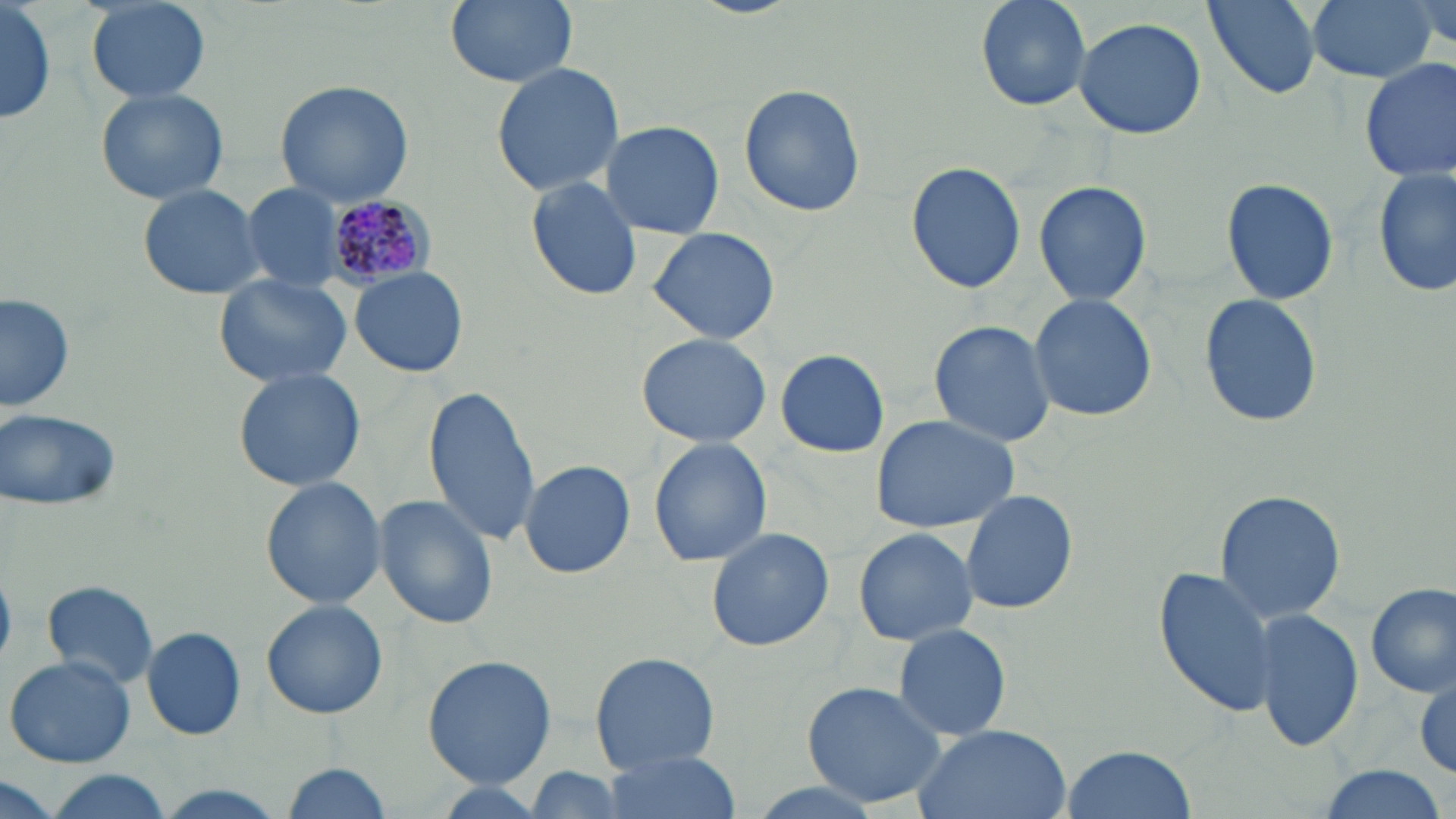
Summary:
  - Coordinate format: approximate bounding boxes as (x1,y1)-(x2,y2) corner pairs in pixels
  - Uninfected red blood cell locations: (1,0)-(56,127), (444,0)-(582,90), (974,0)-(1091,109), (1203,0)-(1327,98), (1303,0)-(1440,84), (1407,0)-(1453,52), (84,1)-(212,104), (1072,16)-(1209,138), (1358,57)-(1455,184), (489,60)-(625,199), (274,78)-(415,208), (737,85)-(867,218), (94,86)-(229,206), (599,120)-(725,239), (906,161)-(1026,292), (1372,168)-(1455,298), (525,175)-(645,303), (1220,176)-(1340,306), (1033,179)-(1153,307), (136,181)-(269,301), (239,183)-(353,292), (647,226)-(780,346), (350,266)-(470,378), (212,275)-(355,389), (2,291)-(75,417), (1026,293)-(1159,423), (1198,293)-(1323,430), (927,319)-(1058,446), (635,333)-(772,448), (774,349)-(889,458), (231,366)-(368,494), (423,386)-(542,547), (2,408)-(122,513), (869,413)-(1021,534), (648,437)-(773,568), (519,459)-(635,578), (260,476)-(386,609), (1213,488)-(1347,623), (958,489)-(1078,615), (374,494)-(498,630), (852,526)-(979,647), (704,527)-(835,652), (1153,565)-(1280,718), (42,579)-(159,690), (1365,582)-(1456,698), (261,599)-(388,718), (1253,606)-(1363,754), (892,623)-(1012,742), (141,626)-(246,740), (589,651)-(722,773), (6,655)-(136,768), (422,655)-(556,788), (1411,669)-(1456,779), (799,678)-(952,810), (911,724)-(1072,819), (1058,746)-(1198,819), (597,751)-(737,819), (280,762)-(397,818), (520,766)-(633,818), (1310,766)-(1453,819), (33,771)-(176,819), (0,776)-(67,819)
  - Plasmodium malariae-infected red blood cell locations: (326,193)-(435,288)
  - Slide-level diagnosis: Plasmodium malariae
  - Preparation: thin blood film
  - Field of view: one of a larger specimen
  - Stain: May-Grünwald-Giemsa
  - Magnification: 1000x
  - Modality: light microscopy
  - Image size: 1456×819 pixels